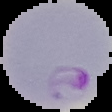
Summary:
  - Malaria status: parasitized
  - Image type: segmented cell region with the area outside set to black
  - Preparation: thin blood film
  - Image size: 112×112 pixels